Identify the parasite.
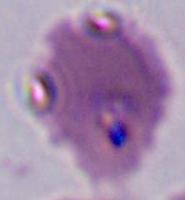
Plasmodium.

Summary:
  - Modality: micrograph
  - Magnification: 400x or 1000x